Classify this cell by malaria status.
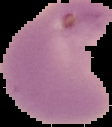
Parasitized.

Summary:
  - Preparation: thin blood film
  - Image type: segmented cell region on a black background
  - Image size: 112×127 pixels